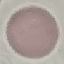

Result: negative for malaria parasites. Acquired by smartphone through the microscope eyepiece. Giemsa stain. Thin blood film. Cell patch, automatically extracted from a larger field of view and resized to 64 × 64 pixels.